Outline each Plasmodium falciparum-infected red blood cell.
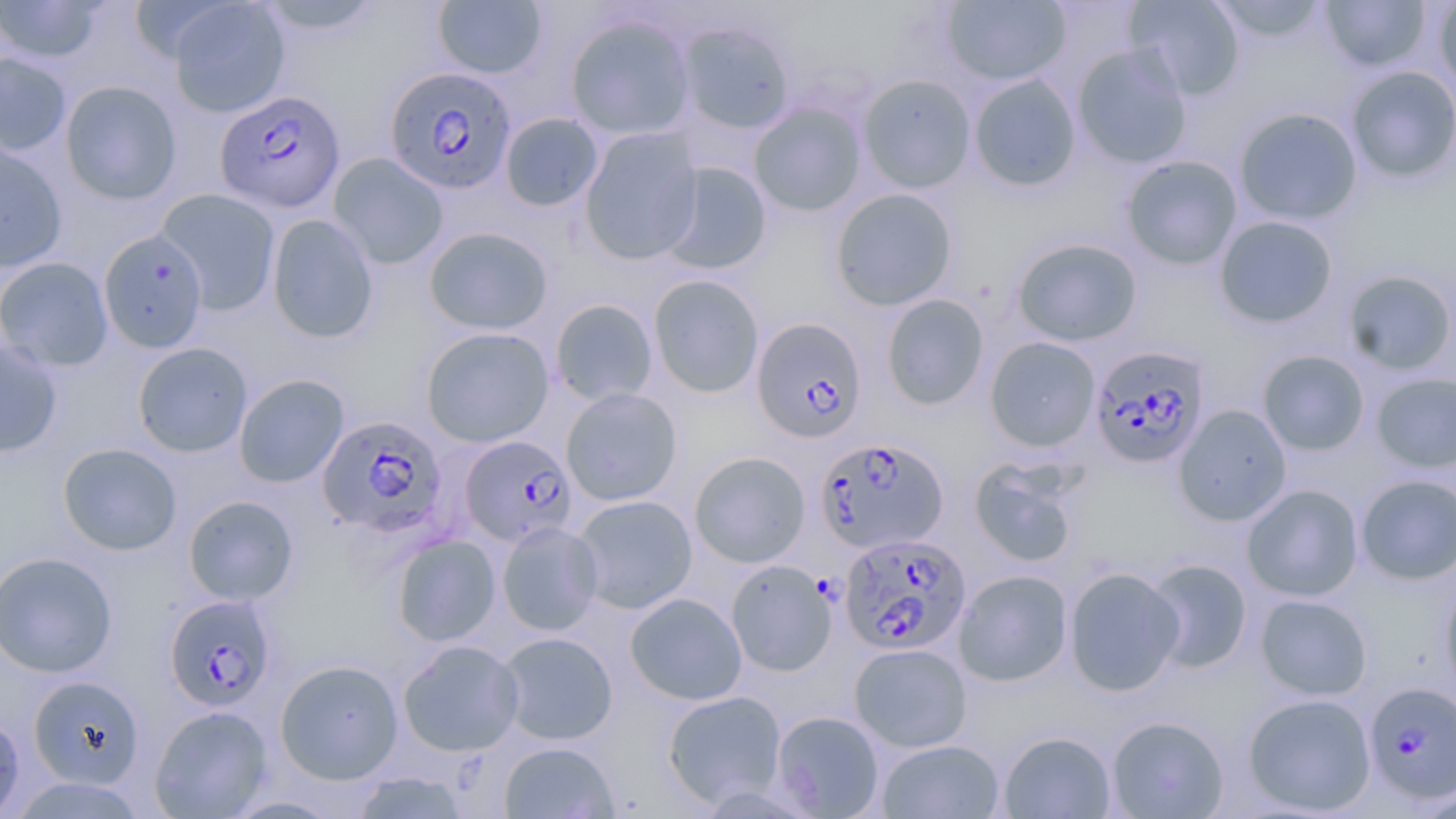
Approximate bounding boxes as (x1, y1, x2, y2) in pixels.
Plasmodium falciparum-infected red blood cells: (384, 67, 517, 195), (212, 86, 343, 210), (752, 317, 867, 443), (1087, 345, 1208, 468), (317, 415, 448, 539), (460, 435, 577, 547), (816, 437, 949, 554), (839, 533, 971, 655), (164, 594, 277, 711), (1363, 680, 1456, 804).

Summary:
  - Uninfected red blood cell locations: (0, 0, 106, 63), (942, 0, 1071, 87), (1125, 0, 1246, 100), (1207, 0, 1332, 44), (1320, 0, 1431, 73), (1432, 0, 1456, 91), (252, 1, 387, 37), (432, 1, 548, 79), (166, 2, 290, 118), (565, 13, 695, 140), (677, 20, 795, 135), (1072, 44, 1193, 169), (0, 52, 73, 156), (1345, 66, 1456, 184), (968, 73, 1082, 193), (858, 74, 976, 193), (60, 80, 182, 205), (749, 102, 866, 217), (1234, 107, 1363, 226), (499, 112, 604, 212), (579, 127, 702, 265), (0, 142, 68, 273), (328, 152, 449, 269), (1121, 155, 1243, 270), (657, 162, 772, 276), (156, 188, 281, 315), (830, 188, 958, 311), (266, 213, 380, 344), (1214, 215, 1338, 328), (424, 225, 554, 335), (98, 229, 208, 352), (1011, 237, 1142, 347), (0, 256, 114, 372), (1342, 269, 1456, 376), (648, 274, 765, 398), (881, 293, 989, 411), (550, 298, 659, 406), (421, 326, 554, 447), (985, 337, 1101, 452), (0, 339, 63, 459), (132, 341, 253, 457), (1258, 349, 1370, 456), (1371, 372, 1456, 472), (233, 373, 350, 488), (561, 387, 682, 506), (1174, 404, 1292, 526), (57, 442, 182, 555), (688, 451, 811, 568), (969, 458, 1081, 568), (1356, 473, 1456, 584), (1242, 484, 1364, 602), (183, 495, 299, 606), (571, 495, 697, 614), (496, 521, 603, 635), (392, 534, 502, 646), (0, 551, 118, 678), (1143, 558, 1252, 674), (726, 560, 837, 676), (1063, 566, 1184, 696), (954, 569, 1073, 687), (1440, 574, 1456, 702), (625, 592, 748, 705), (1255, 594, 1372, 700), (496, 631, 618, 745), (398, 640, 524, 757), (849, 643, 972, 752), (275, 659, 404, 784), (29, 676, 144, 788), (662, 690, 787, 808), (1242, 692, 1376, 815), (150, 705, 273, 818), (772, 711, 885, 818), (0, 714, 25, 818), (1106, 715, 1230, 818), (998, 730, 1117, 818), (877, 739, 1005, 819), (498, 741, 620, 819), (351, 772, 472, 818), (221, 794, 345, 818)
  - Slide-level diagnosis: Plasmodium falciparum
  - Modality: optical microscopy
  - Stain: May-Grünwald-Giemsa
  - Image size: 1456×819 pixels
  - Magnification: 1000x
  - Preparation: thin blood film
  - Field of view: single